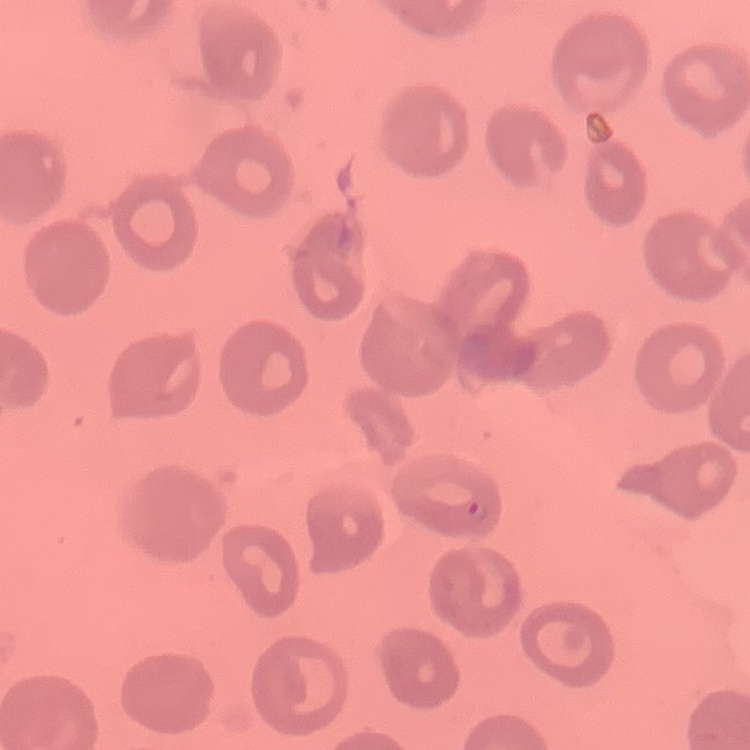
The red blood cells exhibit no rouleaux formation. Square crop of a larger photomicrograph. Thin blood smear. Field's or Giemsa stain.